Classify this cell by malaria status.
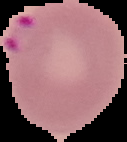

It is parasitized.

{
  "image_size": "127×142 pixels",
  "preparation": "thin blood film",
  "image_type": "cell region segmented out of the field of view; surrounding area masked to black"
}